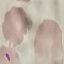

Summary:
  - Malaria status: parasitized
  - Stain: Giemsa
  - Capture: smartphone through the microscope eyepiece
  - Image type: automatically extracted cell patch, resized to 64 × 64 pixels
  - Preparation: thin smear